State which parasite is depicted.
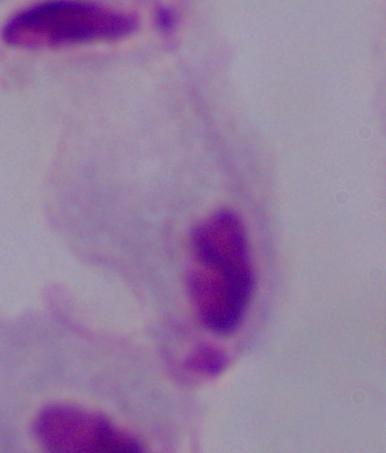

This is a trichomonad.

magnification = 1000x
modality = photomicrograph